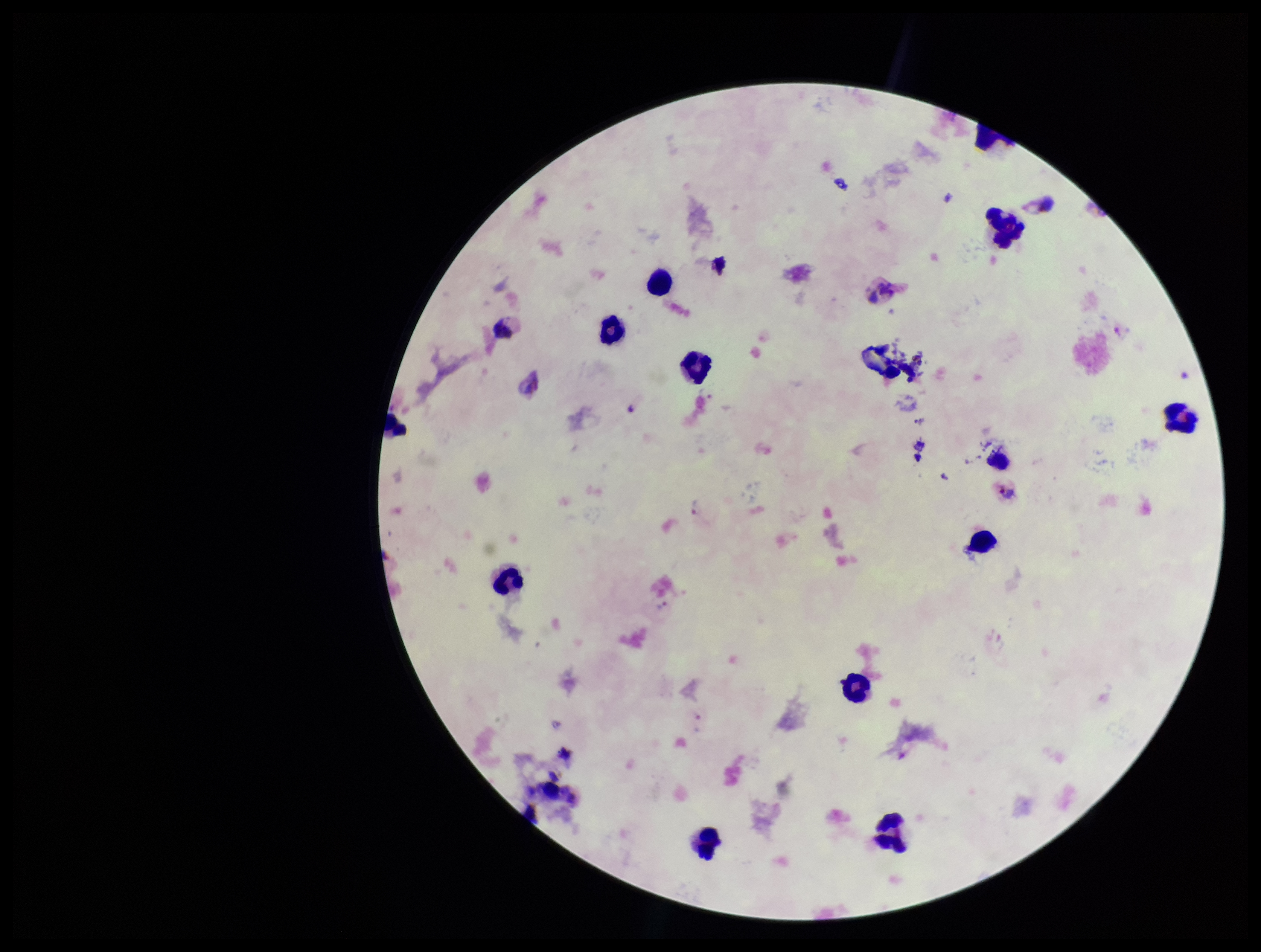
Summary:
  - Preparation: thick blood smear
  - Plasmodium parasites: detected
  - Parasite count: 1
  - Patient malaria status: positive
  - Stain: Giemsa
  - Capture: smartphone photograph through the microscope eyepiece
  - Field of view: single
  - Image size: 1261×952 pixels
  - Leukocyte count: 15
  - Species reported for this patient: Plasmodium vivax